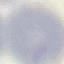
Summary:
  - Malaria status: uninfected
  - Stain: Giemsa
  - Capture: smartphone through the microscope eyepiece
  - Preparation: thin blood film
  - Image type: cell patch, automatically extracted from a larger field of view and resized to 64 × 64 pixels